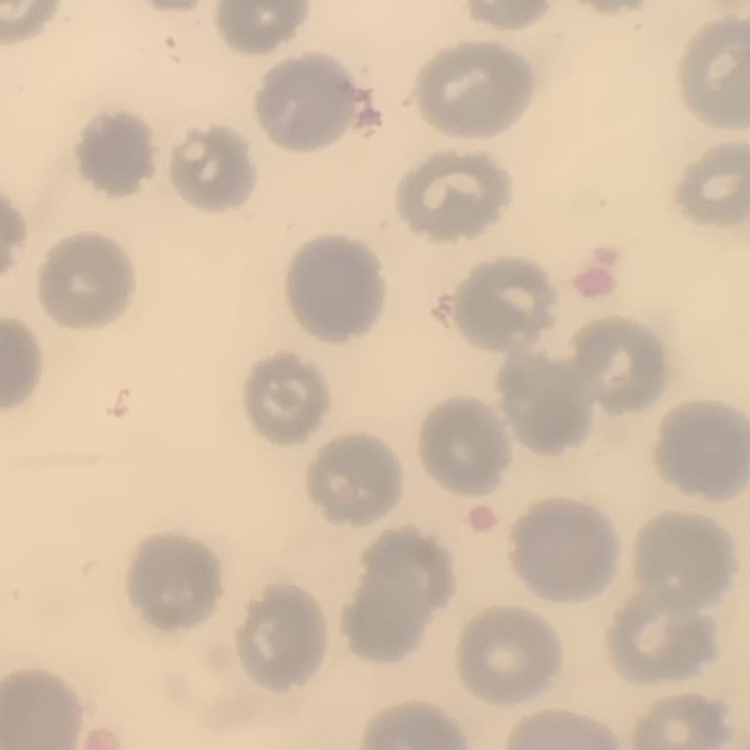
Summary:
  - Erythrocyte morphology: no rouleaux formation
  - Image type: square crop of a larger photomicrograph
  - Stain: Field's or Giemsa
  - Preparation: thin blood film